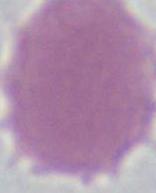

An erythrocyte is shown. Captured at 1000x magnification. Micrograph.